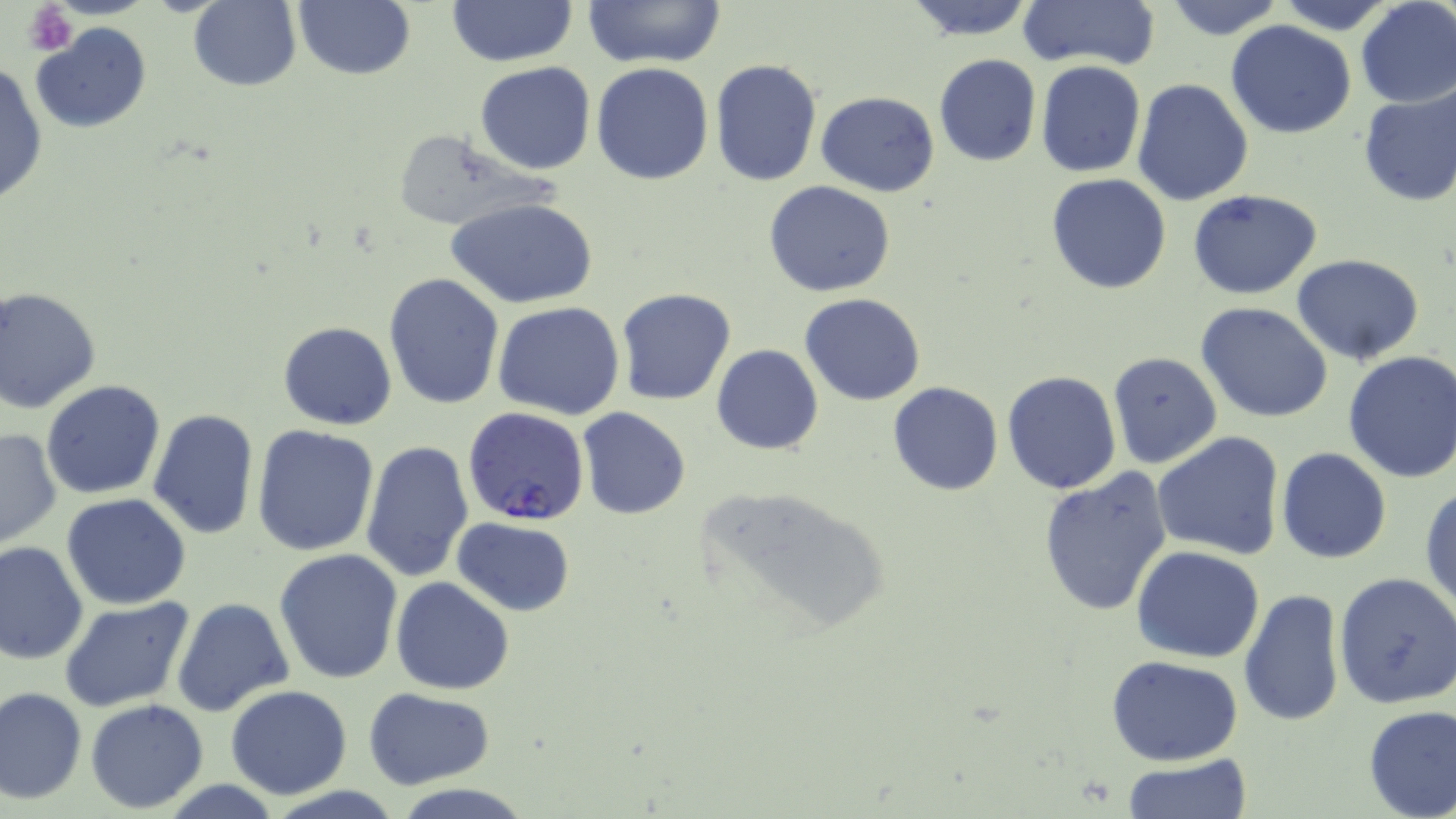 Approximate bounding boxes as named x1/y1/x2/y2 corners in pixels. Plasmodium falciparum-infected red blood cell locations: (x1=464, y1=410, x2=590, y2=526). Uninfected red blood cell locations: (x1=188, y1=0, x2=302, y2=91), (x1=295, y1=0, x2=414, y2=81), (x1=446, y1=0, x2=578, y2=67), (x1=580, y1=0, x2=729, y2=68), (x1=900, y1=0, x2=1040, y2=41), (x1=1014, y1=0, x2=1162, y2=73), (x1=1157, y1=0, x2=1288, y2=40), (x1=1268, y1=0, x2=1403, y2=33), (x1=1354, y1=0, x2=1456, y2=107), (x1=1225, y1=21, x2=1357, y2=139), (x1=33, y1=23, x2=153, y2=136), (x1=934, y1=53, x2=1041, y2=167), (x1=1, y1=59, x2=46, y2=208), (x1=712, y1=59, x2=822, y2=187), (x1=476, y1=61, x2=596, y2=175), (x1=1035, y1=61, x2=1146, y2=177), (x1=591, y1=62, x2=714, y2=185), (x1=1133, y1=79, x2=1254, y2=205), (x1=1356, y1=83, x2=1456, y2=207), (x1=817, y1=90, x2=941, y2=196), (x1=385, y1=128, x2=557, y2=233), (x1=1046, y1=173, x2=1173, y2=294), (x1=763, y1=180, x2=896, y2=297), (x1=1188, y1=188, x2=1323, y2=300), (x1=451, y1=199, x2=596, y2=310), (x1=1291, y1=254, x2=1424, y2=365), (x1=384, y1=273, x2=506, y2=411), (x1=0, y1=285, x2=103, y2=412), (x1=615, y1=288, x2=738, y2=406), (x1=800, y1=293, x2=927, y2=406), (x1=494, y1=301, x2=625, y2=420), (x1=1196, y1=302, x2=1333, y2=423), (x1=279, y1=321, x2=397, y2=430), (x1=712, y1=345, x2=823, y2=454), (x1=1341, y1=350, x2=1456, y2=485), (x1=1107, y1=352, x2=1223, y2=469), (x1=1001, y1=372, x2=1120, y2=494), (x1=41, y1=379, x2=166, y2=499), (x1=887, y1=383, x2=1003, y2=496), (x1=577, y1=406, x2=692, y2=521), (x1=148, y1=408, x2=261, y2=541), (x1=252, y1=426, x2=378, y2=557), (x1=0, y1=428, x2=62, y2=551), (x1=1153, y1=430, x2=1285, y2=560), (x1=360, y1=440, x2=475, y2=583), (x1=1276, y1=447, x2=1392, y2=564), (x1=1037, y1=468, x2=1173, y2=619), (x1=697, y1=483, x2=890, y2=641), (x1=1420, y1=483, x2=1455, y2=614), (x1=61, y1=493, x2=192, y2=609), (x1=451, y1=517, x2=579, y2=617), (x1=0, y1=541, x2=88, y2=665), (x1=1132, y1=546, x2=1265, y2=663), (x1=274, y1=547, x2=403, y2=684), (x1=1333, y1=570, x2=1456, y2=710), (x1=391, y1=577, x2=514, y2=694), (x1=1239, y1=589, x2=1346, y2=726), (x1=60, y1=597, x2=196, y2=714), (x1=171, y1=598, x2=294, y2=717), (x1=1107, y1=656, x2=1243, y2=766), (x1=224, y1=685, x2=353, y2=799), (x1=1, y1=686, x2=87, y2=804), (x1=363, y1=688, x2=495, y2=789), (x1=85, y1=699, x2=208, y2=815), (x1=1360, y1=704, x2=1456, y2=818), (x1=1121, y1=757, x2=1253, y2=819), (x1=393, y1=783, x2=534, y2=819). Platelet locations: (x1=24, y1=1, x2=78, y2=56). Slide-level diagnosis: Plasmodium falciparum. 1000x magnification. One field of a larger specimen. May-Grünwald-Giemsa-stained preparation. Image is 1456×819 pixels. Light microscopy. Thin blood smear.